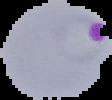 Malaria status: parasitized. Image is 112×100 pixels. Segmented cell region on a black background. From a thin blood film.